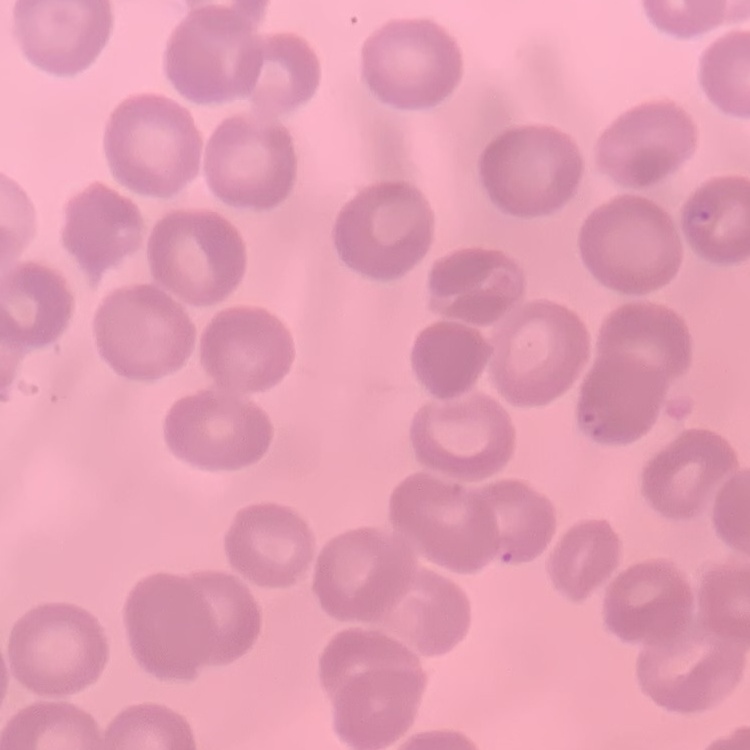

red blood cell morphology = no rouleaux formation
image type = one tile cut from a larger photomicrograph
preparation = thin blood film
stain = Field's or Giemsa